Describe the morphology of the erythrocytes.
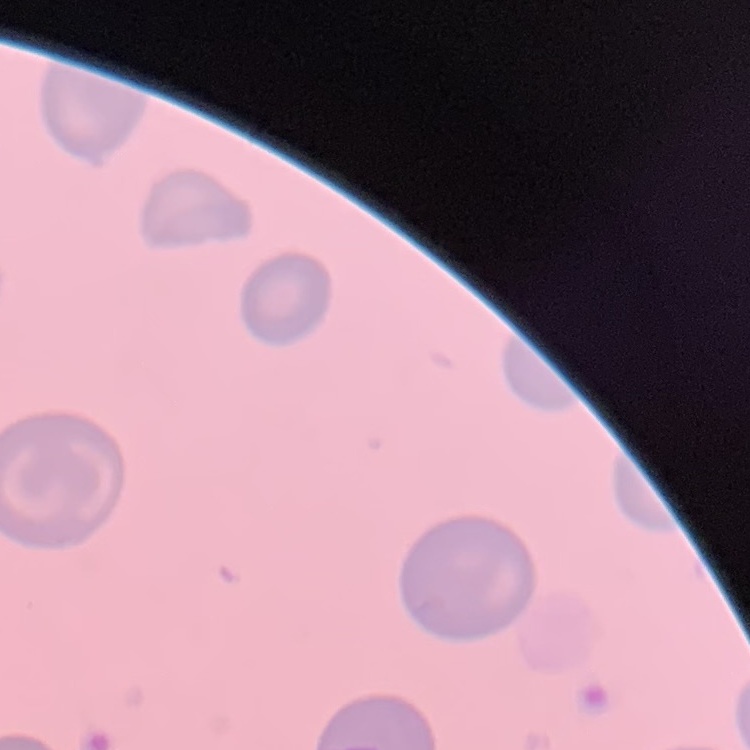

They show no rouleaux formation.

Thin peripheral smear. Field's or Giemsa stain. Square crop of a larger photomicrograph.